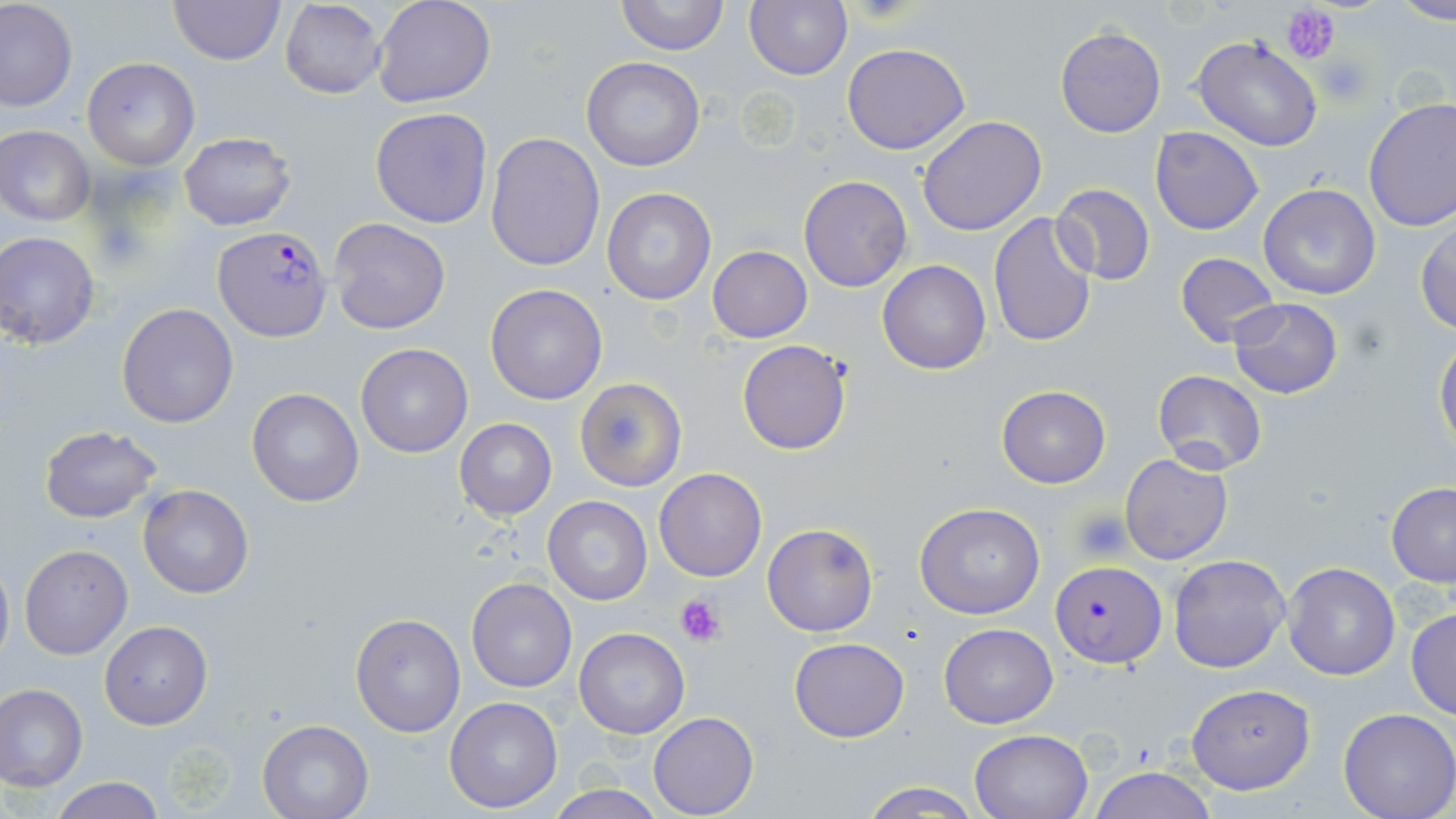 Approximate bounding boxes as named x1/y1/x2/y2 corners in pixels. Plasmodium falciparum-infected red blood cell locations: (x1=213, y1=225, x2=331, y2=340), (x1=1052, y1=561, x2=1164, y2=668). Platelet locations: (x1=1283, y1=4, x2=1339, y2=64), (x1=1314, y1=51, x2=1375, y2=106), (x1=1071, y1=508, x2=1132, y2=561), (x1=675, y1=593, x2=728, y2=648). Uninfected red blood cell locations: (x1=168, y1=0, x2=286, y2=66), (x1=371, y1=0, x2=496, y2=108), (x1=615, y1=0, x2=729, y2=55), (x1=743, y1=0, x2=851, y2=81), (x1=1390, y1=0, x2=1456, y2=25), (x1=280, y1=1, x2=387, y2=100), (x1=1, y1=2, x2=77, y2=112), (x1=1055, y1=26, x2=1166, y2=137), (x1=1191, y1=35, x2=1323, y2=152), (x1=842, y1=42, x2=971, y2=154), (x1=82, y1=57, x2=199, y2=169), (x1=581, y1=57, x2=706, y2=171), (x1=1362, y1=97, x2=1456, y2=232), (x1=370, y1=107, x2=493, y2=230), (x1=918, y1=115, x2=1048, y2=236), (x1=1, y1=125, x2=95, y2=224), (x1=1151, y1=126, x2=1264, y2=235), (x1=484, y1=130, x2=604, y2=271), (x1=178, y1=131, x2=299, y2=231), (x1=798, y1=175, x2=914, y2=292), (x1=1049, y1=182, x2=1156, y2=286), (x1=1257, y1=183, x2=1382, y2=299), (x1=602, y1=187, x2=716, y2=305), (x1=988, y1=213, x2=1098, y2=349), (x1=327, y1=217, x2=450, y2=334), (x1=1415, y1=217, x2=1456, y2=334), (x1=1, y1=232, x2=103, y2=349), (x1=707, y1=246, x2=813, y2=343), (x1=1173, y1=253, x2=1281, y2=347), (x1=877, y1=260, x2=992, y2=375), (x1=484, y1=283, x2=608, y2=404), (x1=1228, y1=296, x2=1344, y2=399), (x1=116, y1=303, x2=239, y2=429), (x1=1433, y1=338, x2=1456, y2=452), (x1=738, y1=339, x2=852, y2=454), (x1=356, y1=343, x2=472, y2=457), (x1=1152, y1=369, x2=1267, y2=476), (x1=574, y1=377, x2=687, y2=492), (x1=995, y1=386, x2=1110, y2=488), (x1=246, y1=387, x2=365, y2=508), (x1=455, y1=419, x2=556, y2=521), (x1=38, y1=424, x2=163, y2=523), (x1=1121, y1=452, x2=1233, y2=564), (x1=653, y1=467, x2=768, y2=582), (x1=1385, y1=482, x2=1456, y2=586), (x1=137, y1=485, x2=253, y2=598), (x1=543, y1=496, x2=652, y2=604), (x1=915, y1=501, x2=1046, y2=619), (x1=762, y1=522, x2=880, y2=637), (x1=20, y1=544, x2=131, y2=660), (x1=0, y1=553, x2=13, y2=669), (x1=1169, y1=554, x2=1293, y2=674), (x1=1282, y1=562, x2=1398, y2=679), (x1=466, y1=575, x2=577, y2=692), (x1=1405, y1=607, x2=1456, y2=719), (x1=350, y1=613, x2=465, y2=736), (x1=99, y1=619, x2=212, y2=730), (x1=939, y1=623, x2=1058, y2=729), (x1=573, y1=627, x2=689, y2=739), (x1=789, y1=637, x2=909, y2=742), (x1=1184, y1=683, x2=1316, y2=794), (x1=0, y1=684, x2=87, y2=793), (x1=444, y1=696, x2=564, y2=812), (x1=1338, y1=708, x2=1455, y2=819), (x1=648, y1=711, x2=759, y2=818), (x1=257, y1=718, x2=374, y2=819), (x1=968, y1=728, x2=1093, y2=819), (x1=1084, y1=767, x2=1218, y2=819), (x1=47, y1=777, x2=168, y2=819), (x1=857, y1=779, x2=983, y2=818), (x1=545, y1=786, x2=669, y2=819). Slide-level diagnosis: Plasmodium falciparum. Image is 1456×819 pixels. Thin blood smear. Captured at 1000x magnification. May-Grünwald-Giemsa-stained preparation. Optical microscopy. One field of a larger specimen.